Report the malaria status of this cell.
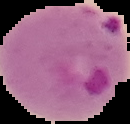
Parasitized.

From a thin blood film. Image is 130×124 pixels. The area outside the segmented cell region is set to black.